Report the malaria status of this cell.
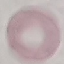

It is uninfected.

Acquired by smartphone through the microscope eyepiece. Giemsa-stained preparation. Thin blood film. Cell patch, automatically extracted from a larger field of view and resized to 64 × 64 pixels.